Assess this cell for malaria.
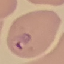

It is parasitized.

Summary:
  - Stain: Giemsa
  - Capture: smartphone camera at the microscope eyepiece
  - Image type: cell patch, automatically extracted from a larger field of view and resized to 64 × 64 pixels
  - Preparation: thin blood smear